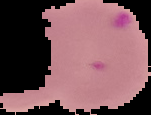
Summary:
  - Image size: 151×115 pixels
  - Malaria status: parasitized
  - Preparation: thin blood smear
  - Image type: segmented cell region on a black background